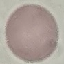 Result: no malaria parasites detected. Giemsa-stained preparation. Thin smear of blood. Photographed with a smartphone camera at the microscope eyepiece. Cell patch, automatically extracted from a larger field of view and resized to 64 × 64 pixels.